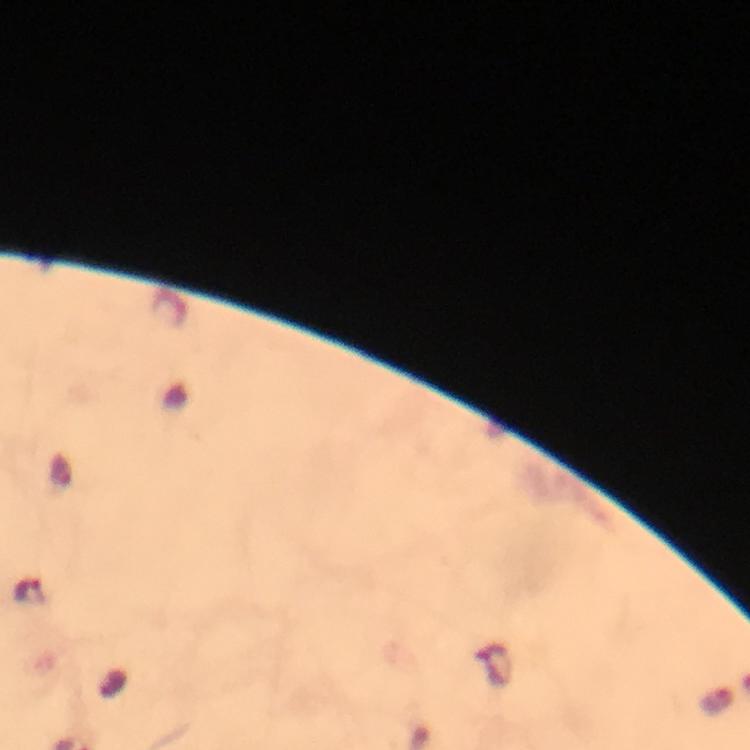

{
  "magnification": "100x",
  "cropped_from": "a single field of view",
  "capture": "smartphone camera through the microscope",
  "immersion_oil": "used",
  "context": "from a malaria diagnostic workup",
  "preparation": "thick smear",
  "malaria_parasite_locations": "approximate object centers, in pixels from the top-left corner: (x=30, y=593)",
  "stain": "Giemsa",
  "image_size": "750×750 pixels"
}